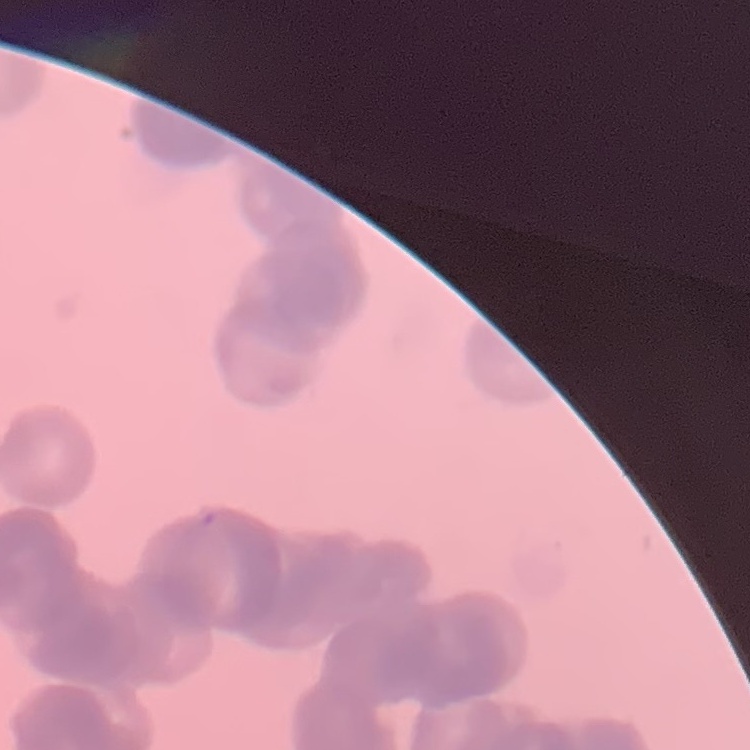

Summary:
  - Red blood cell morphology: rouleaux formation
  - Stain: Field's or Giemsa
  - Preparation: thin blood film
  - Image type: one tile cut from a larger photomicrograph